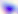

{
  "identification": "Toxoplasma gondii",
  "magnification": "400x",
  "modality": "photomicrograph"
}